Outline each Plasmodium falciparum-infected red blood cell.
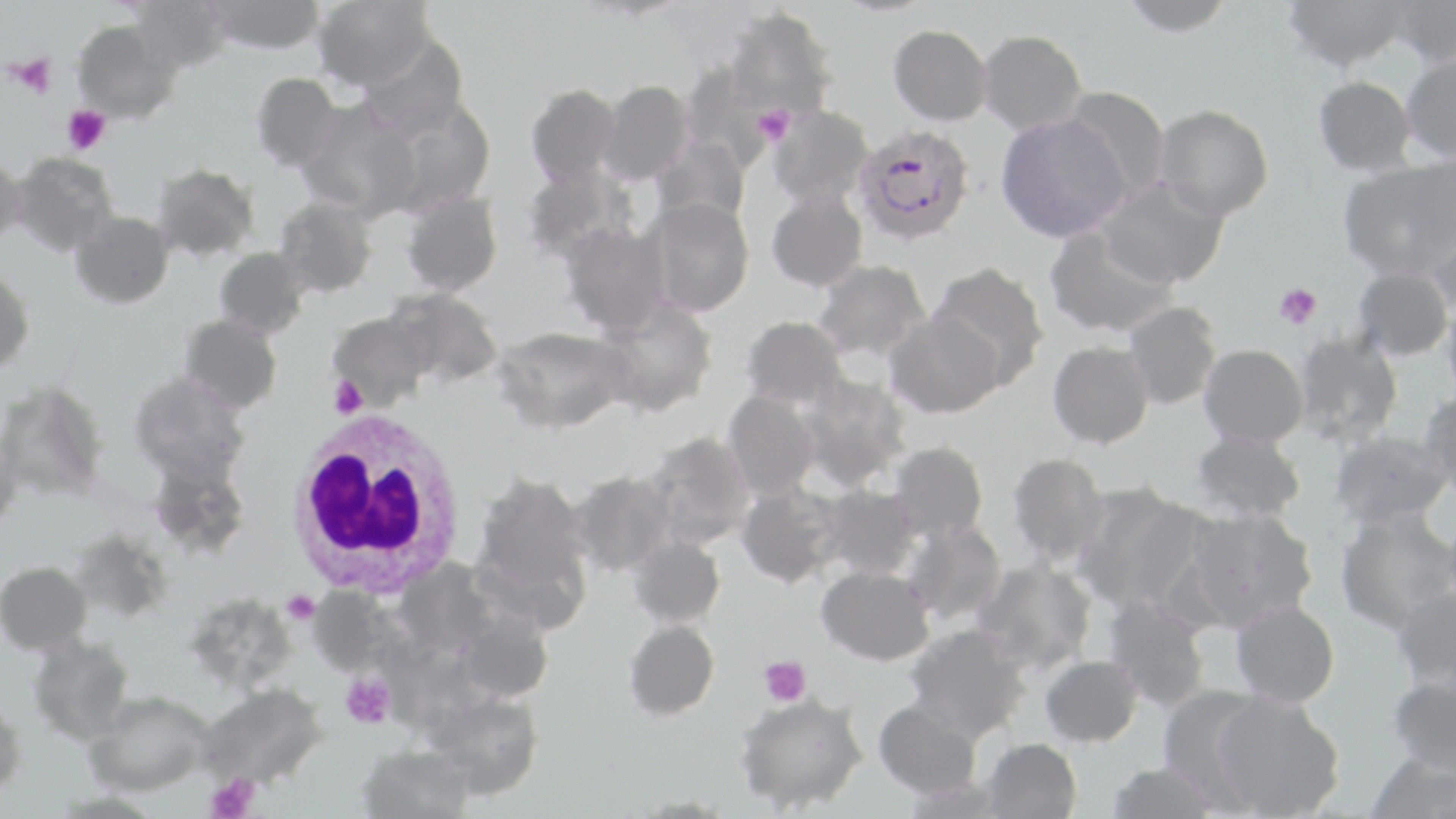
Approximate bounding boxes as (x1,y1)-(x2,y2) corner pairs in pixels.
Plasmodium falciparum-infected red blood cells: (857,130)-(973,247).

Summary:
  - Uninfected red blood cell locations: (127,0)-(232,75), (202,0)-(326,55), (313,0)-(436,89), (1119,0)-(1235,37), (1283,0)-(1411,71), (1387,0)-(1456,68), (724,7)-(838,119), (72,21)-(180,123), (889,24)-(993,125), (978,29)-(1087,135), (357,32)-(470,139), (1400,53)-(1456,163), (679,61)-(776,166), (250,72)-(342,172), (1314,75)-(1416,176), (598,79)-(695,185), (525,83)-(622,186), (1061,85)-(1170,201), (381,98)-(498,217), (295,99)-(422,221), (1154,104)-(1274,220), (767,105)-(875,208), (995,114)-(1130,243), (650,135)-(751,228), (0,152)-(24,250), (9,152)-(118,257), (1338,160)-(1455,280), (152,163)-(259,261), (521,165)-(638,266), (1098,178)-(1228,289), (400,189)-(504,296), (766,190)-(867,292), (274,195)-(378,298), (644,197)-(754,317), (69,210)-(174,308), (1428,220)-(1456,322), (560,223)-(670,336), (1045,225)-(1179,338), (213,247)-(310,339), (812,258)-(931,362), (929,261)-(1050,389), (0,265)-(35,376), (1352,267)-(1452,361), (385,287)-(504,388), (593,297)-(719,418), (1441,300)-(1456,403), (1122,301)-(1222,410), (884,311)-(1004,419), (327,312)-(432,411), (180,314)-(282,414), (741,315)-(849,411), (493,325)-(630,434), (1292,329)-(1404,447), (1047,341)-(1154,448), (1199,344)-(1308,447), (129,371)-(251,486), (795,375)-(912,491), (0,380)-(110,502), (722,390)-(820,499), (1419,390)-(1456,496), (1189,430)-(1306,522), (1329,430)-(1452,528), (643,431)-(756,549), (0,432)-(22,533), (888,441)-(989,543), (1007,452)-(1110,566), (148,460)-(252,558), (569,471)-(676,576), (475,474)-(591,593), (735,481)-(844,589), (818,485)-(921,580), (1071,485)-(1205,612), (1181,507)-(1318,630), (1335,510)-(1456,635), (901,520)-(1007,625), (626,535)-(725,629), (394,559)-(499,656), (973,560)-(1097,674), (0,561)-(91,655), (816,566)-(935,666), (308,587)-(399,677), (1391,587)-(1456,693), (185,591)-(297,691), (1103,596)-(1211,713), (1230,600)-(1340,707), (451,607)-(554,704), (624,619)-(720,721), (906,624)-(1030,743), (28,635)-(135,744), (1040,655)-(1142,747), (1387,674)-(1456,777), (198,683)-(327,789), (1157,685)-(1267,804), (83,690)-(214,796), (422,691)-(543,799), (1212,691)-(1345,818), (734,692)-(868,813), (0,698)-(27,799), (874,699)-(982,800), (981,737)-(1082,819), (357,744)-(476,818), (1363,752)-(1455,819), (1107,762)-(1221,819)
  - Platelet locations: (11,53)-(57,99), (63,105)-(110,154), (752,107)-(794,145), (1274,283)-(1322,329), (329,374)-(369,419), (281,589)-(320,625), (759,656)-(811,706), (341,673)-(396,728), (205,774)-(261,819)
  - White blood cell locations: (285,410)-(470,599)
  - Slide-level diagnosis: Plasmodium falciparum
  - Magnification: 1000x
  - Image size: 1456×819 pixels
  - Field of view: one of a larger specimen
  - Modality: light microscopy
  - Stain: May-Grünwald-Giemsa
  - Preparation: thin blood smear